Describe the morphology of the red blood cells.
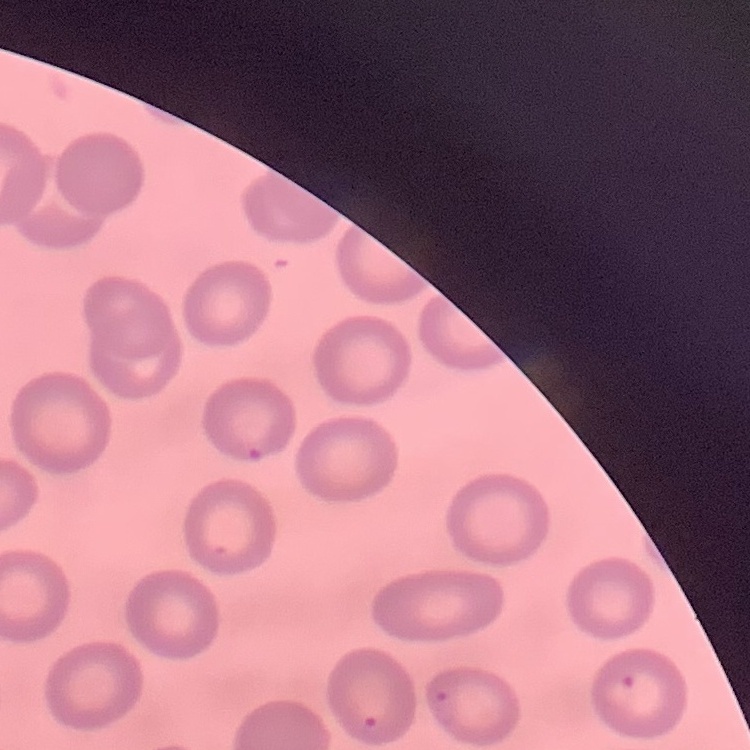
They show no rouleaux formation.

One tile cut from a larger photomicrograph. Field's or Giemsa stain. Thin peripheral smear.